Classify this cell by malaria status.
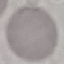

It is uninfected.

Summary:
  - Image type: cell patch, automatically extracted from a larger field of view and resized to 64 × 64 pixels
  - Stain: Giemsa
  - Preparation: thin smear
  - Capture: smartphone camera at the microscope eyepiece